Describe the morphology of the erythrocytes.
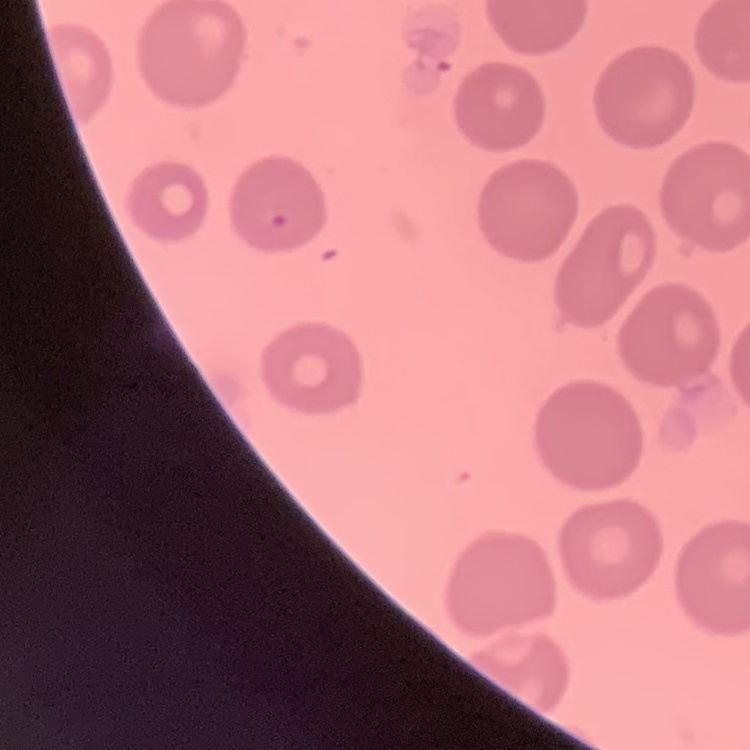

No rouleaux formation.

image type = square crop of a larger photomicrograph
stain = Field's or Giemsa
preparation = thin blood smear